Give the extent of all Babesia divergens-infected red blood cells.
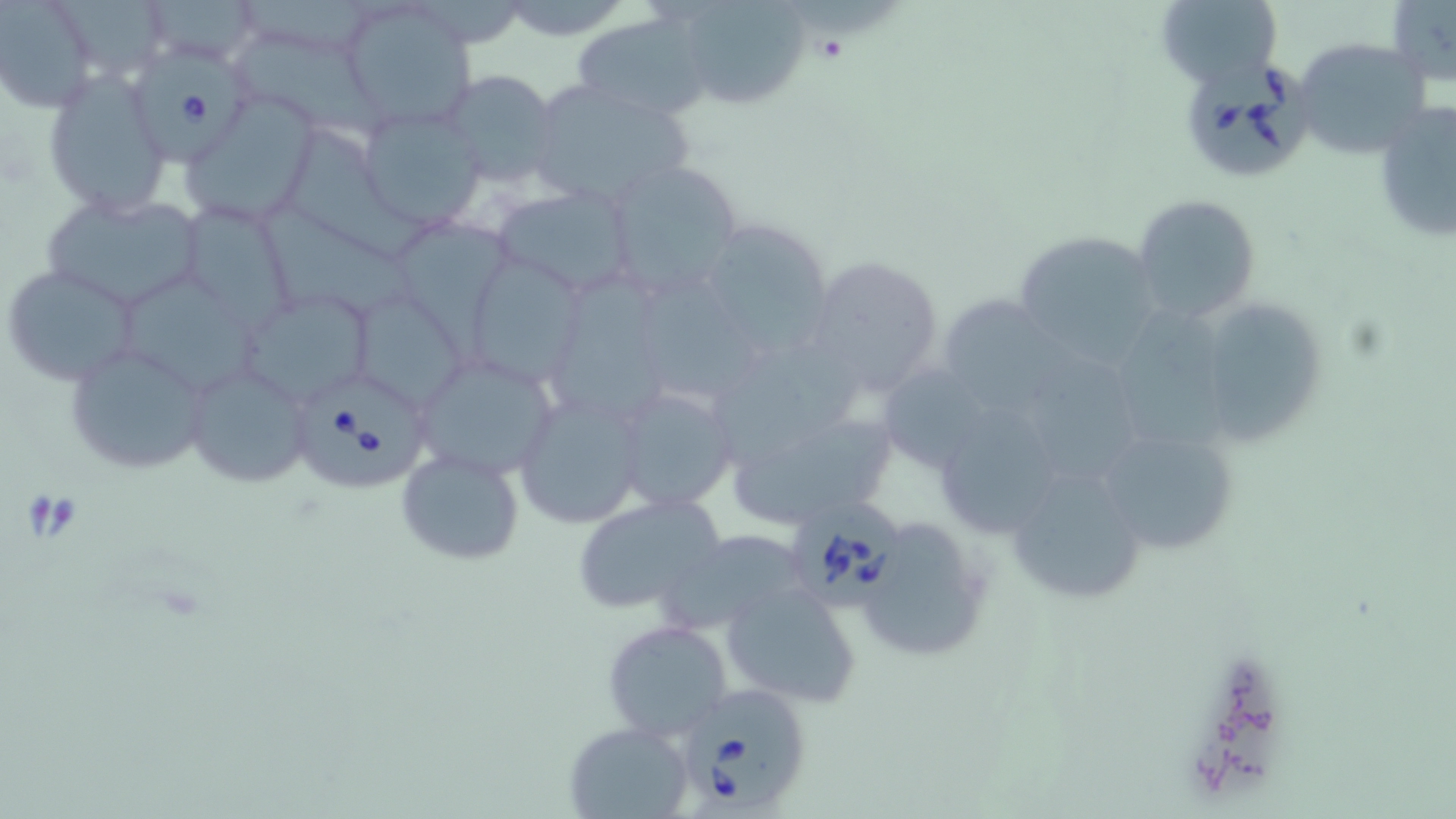
Approximate bounding boxes as [x1, y1, x2, y2] in pixels.
Babesia divergens-infected red blood cells: [137, 50, 247, 167], [1182, 62, 1310, 179], [298, 376, 431, 492], [792, 502, 904, 605], [685, 682, 811, 807].

Uninfected red blood cell locations: [141, 0, 261, 67], [1154, 0, 1283, 88], [1386, 0, 1456, 89], [676, 1, 813, 110], [0, 2, 97, 113], [340, 4, 480, 127], [572, 12, 714, 120], [1304, 47, 1434, 158], [248, 48, 389, 141], [40, 67, 176, 219], [442, 70, 560, 186], [523, 80, 696, 207], [182, 94, 324, 224], [1373, 99, 1456, 246], [361, 106, 487, 231], [283, 132, 443, 264], [603, 159, 747, 298], [491, 183, 632, 296], [37, 191, 206, 313], [1132, 195, 1261, 323], [176, 200, 299, 334], [261, 203, 424, 317], [387, 218, 520, 372], [698, 220, 837, 360], [1013, 230, 1162, 363], [802, 252, 948, 403], [473, 256, 581, 393], [3, 265, 142, 386], [551, 269, 679, 426], [636, 271, 775, 405], [119, 276, 275, 402], [352, 290, 468, 410], [245, 295, 370, 402], [936, 295, 1073, 421], [1209, 301, 1323, 449], [1119, 312, 1243, 452], [66, 343, 210, 478], [1025, 343, 1151, 487], [724, 346, 867, 464], [411, 353, 561, 480], [877, 364, 997, 472], [183, 365, 312, 491], [612, 385, 740, 513], [513, 393, 646, 529], [927, 400, 1069, 538], [723, 401, 901, 530], [1087, 419, 1244, 556], [396, 449, 525, 565], [1005, 464, 1150, 604], [570, 493, 727, 618], [855, 517, 990, 662], [671, 531, 804, 629], [720, 581, 860, 709], [601, 618, 734, 743], [563, 721, 695, 818]. Slide-level diagnosis: Babesia divergens. Light microscopy. May-Grünwald-Giemsa-stained preparation. Image is 1456×819 pixels. One field of a larger specimen. Thin blood smear. Captured at 1000x magnification.